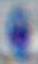
Toxoplasma gondii is seen. Captured at 1000x magnification. Micrograph.